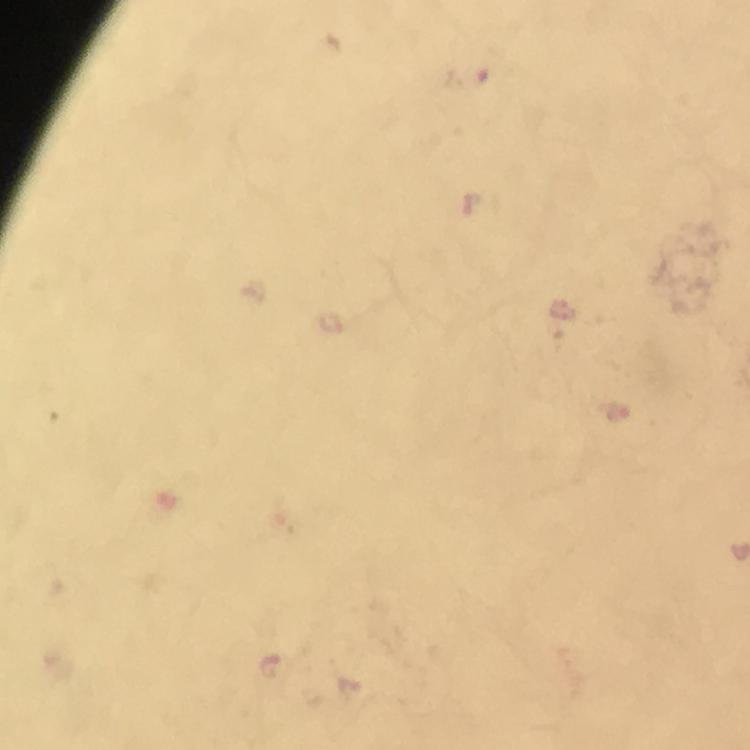

capture = smartphone camera through the microscope
immersion oil = applied
magnification = 100x
stain = Giemsa
image size = 750×750 pixels
cropped from = a single field of view
preparation = thick blood film
malaria parasite locations = approximate object centers, in pixels from the top-left corner: (x=469, y=76)
context = from a malaria diagnostic workup